Report the malaria status of this cell.
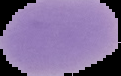
Uninfected.

{
  "image_type": "segmented cell region with the area outside set to black",
  "image_size": "121×76 pixels",
  "preparation": "thin blood smear"
}